Locate every Plasmodium ovale-infected red blood cell.
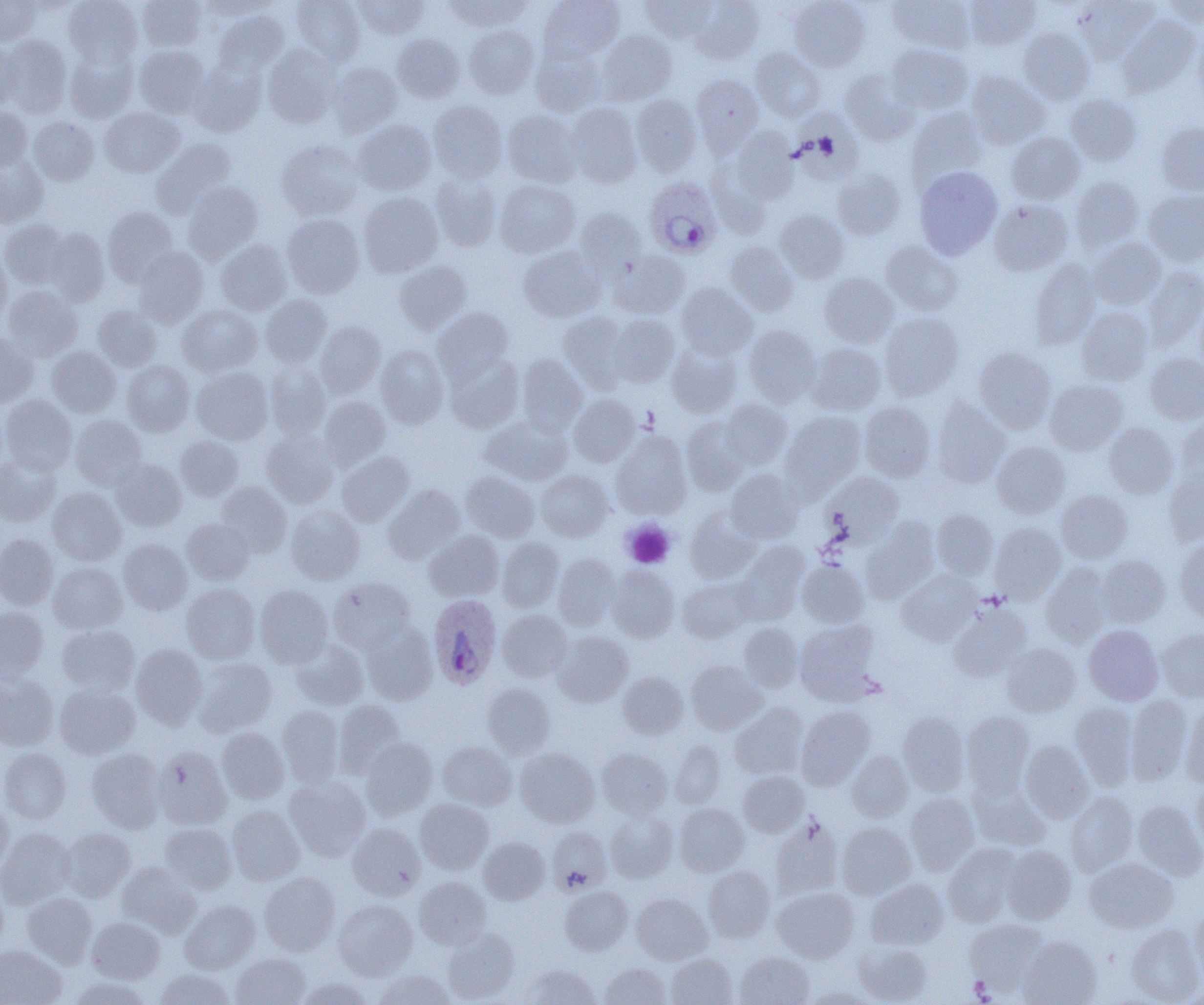
Approximate bounding boxes as named x1/y1/x2/y2 corners in pixels.
Plasmodium ovale-infected red blood cells: (x1=644, y1=177, x2=723, y2=259), (x1=428, y1=594, x2=502, y2=690).

Summary:
  - Platelet locations: (x1=622, y1=520, x2=675, y2=568), (x1=969, y1=976, x2=994, y2=1001)
  - Uninfected red blood cell locations: (x1=0, y1=0, x2=41, y2=44), (x1=64, y1=0, x2=142, y2=67), (x1=201, y1=0, x2=279, y2=20), (x1=292, y1=0, x2=365, y2=65), (x1=353, y1=0, x2=429, y2=39), (x1=446, y1=0, x2=531, y2=31), (x1=539, y1=0, x2=625, y2=61), (x1=641, y1=0, x2=716, y2=42), (x1=690, y1=0, x2=765, y2=63), (x1=888, y1=0, x2=976, y2=54), (x1=964, y1=0, x2=1040, y2=50), (x1=1074, y1=0, x2=1158, y2=63), (x1=1162, y1=0, x2=1204, y2=27), (x1=137, y1=1, x2=207, y2=51), (x1=789, y1=1, x2=870, y2=71), (x1=213, y1=10, x2=289, y2=76), (x1=1118, y1=16, x2=1200, y2=97), (x1=464, y1=25, x2=538, y2=99), (x1=1193, y1=27, x2=1204, y2=104), (x1=1018, y1=28, x2=1094, y2=104), (x1=596, y1=30, x2=677, y2=105), (x1=392, y1=34, x2=464, y2=103), (x1=2, y1=36, x2=72, y2=118), (x1=0, y1=43, x2=22, y2=109), (x1=887, y1=43, x2=973, y2=114), (x1=263, y1=44, x2=343, y2=126), (x1=135, y1=45, x2=210, y2=118), (x1=530, y1=45, x2=605, y2=116), (x1=751, y1=47, x2=826, y2=121), (x1=64, y1=48, x2=138, y2=122), (x1=190, y1=61, x2=266, y2=136), (x1=329, y1=62, x2=403, y2=136), (x1=839, y1=67, x2=919, y2=144), (x1=967, y1=72, x2=1050, y2=149), (x1=691, y1=74, x2=763, y2=153), (x1=631, y1=93, x2=702, y2=176), (x1=1066, y1=93, x2=1141, y2=166), (x1=428, y1=101, x2=507, y2=182), (x1=565, y1=102, x2=643, y2=188), (x1=100, y1=106, x2=185, y2=177), (x1=0, y1=107, x2=32, y2=172), (x1=907, y1=108, x2=988, y2=186), (x1=790, y1=109, x2=865, y2=183), (x1=502, y1=110, x2=581, y2=186), (x1=29, y1=117, x2=99, y2=185), (x1=354, y1=119, x2=437, y2=194), (x1=1157, y1=122, x2=1204, y2=195), (x1=730, y1=127, x2=799, y2=202), (x1=1007, y1=131, x2=1085, y2=204), (x1=151, y1=138, x2=236, y2=217), (x1=277, y1=139, x2=364, y2=219), (x1=0, y1=158, x2=48, y2=227), (x1=707, y1=160, x2=776, y2=238), (x1=914, y1=166, x2=1002, y2=258), (x1=832, y1=169, x2=906, y2=239), (x1=430, y1=173, x2=501, y2=251), (x1=1071, y1=177, x2=1143, y2=252), (x1=494, y1=179, x2=580, y2=258), (x1=183, y1=182, x2=263, y2=262), (x1=1144, y1=188, x2=1204, y2=266), (x1=358, y1=192, x2=443, y2=277), (x1=990, y1=199, x2=1072, y2=275), (x1=102, y1=207, x2=179, y2=284), (x1=574, y1=208, x2=647, y2=280), (x1=774, y1=209, x2=849, y2=281), (x1=282, y1=214, x2=364, y2=298), (x1=0, y1=219, x2=69, y2=288), (x1=44, y1=228, x2=110, y2=305), (x1=1087, y1=237, x2=1166, y2=309), (x1=215, y1=240, x2=292, y2=315), (x1=881, y1=241, x2=964, y2=316), (x1=725, y1=242, x2=798, y2=316), (x1=134, y1=246, x2=208, y2=326), (x1=518, y1=246, x2=604, y2=322), (x1=0, y1=249, x2=11, y2=325), (x1=609, y1=251, x2=690, y2=319), (x1=1029, y1=259, x2=1100, y2=348), (x1=394, y1=260, x2=471, y2=333), (x1=1143, y1=266, x2=1204, y2=349), (x1=819, y1=273, x2=898, y2=347), (x1=676, y1=283, x2=758, y2=359), (x1=3, y1=286, x2=83, y2=360), (x1=261, y1=294, x2=332, y2=367), (x1=1195, y1=300, x2=1204, y2=374), (x1=93, y1=304, x2=162, y2=371), (x1=177, y1=304, x2=261, y2=376), (x1=1077, y1=307, x2=1153, y2=384), (x1=432, y1=308, x2=513, y2=381), (x1=558, y1=311, x2=629, y2=390), (x1=879, y1=312, x2=964, y2=400), (x1=609, y1=315, x2=681, y2=387), (x1=315, y1=321, x2=385, y2=397), (x1=744, y1=325, x2=821, y2=406), (x1=0, y1=333, x2=38, y2=407), (x1=666, y1=342, x2=741, y2=417), (x1=808, y1=343, x2=886, y2=415), (x1=376, y1=344, x2=449, y2=428), (x1=47, y1=346, x2=121, y2=417), (x1=974, y1=347, x2=1056, y2=433), (x1=445, y1=353, x2=524, y2=434), (x1=1145, y1=354, x2=1204, y2=424), (x1=517, y1=355, x2=588, y2=433), (x1=122, y1=360, x2=195, y2=436), (x1=265, y1=361, x2=330, y2=440), (x1=192, y1=367, x2=273, y2=445), (x1=1044, y1=379, x2=1127, y2=455), (x1=569, y1=394, x2=640, y2=466), (x1=1, y1=395, x2=77, y2=474), (x1=318, y1=396, x2=390, y2=470), (x1=932, y1=398, x2=1009, y2=487), (x1=720, y1=399, x2=793, y2=468), (x1=859, y1=401, x2=935, y2=481), (x1=782, y1=411, x2=866, y2=492), (x1=482, y1=415, x2=573, y2=485), (x1=70, y1=416, x2=147, y2=490), (x1=681, y1=416, x2=752, y2=494), (x1=1175, y1=417, x2=1204, y2=489), (x1=1104, y1=422, x2=1178, y2=499), (x1=261, y1=430, x2=340, y2=508), (x1=612, y1=431, x2=691, y2=518), (x1=175, y1=435, x2=243, y2=501), (x1=992, y1=441, x2=1070, y2=518), (x1=337, y1=451, x2=415, y2=526), (x1=0, y1=454, x2=61, y2=526), (x1=111, y1=460, x2=187, y2=531), (x1=726, y1=469, x2=804, y2=543), (x1=1163, y1=469, x2=1204, y2=546), (x1=536, y1=470, x2=613, y2=542), (x1=461, y1=471, x2=540, y2=542), (x1=822, y1=472, x2=903, y2=544), (x1=216, y1=482, x2=292, y2=557), (x1=383, y1=485, x2=465, y2=564), (x1=47, y1=487, x2=127, y2=565), (x1=1057, y1=491, x2=1132, y2=562), (x1=286, y1=505, x2=364, y2=584), (x1=685, y1=509, x2=760, y2=583), (x1=931, y1=509, x2=998, y2=579), (x1=182, y1=518, x2=254, y2=584), (x1=861, y1=520, x2=938, y2=603), (x1=990, y1=522, x2=1066, y2=603), (x1=424, y1=530, x2=504, y2=601), (x1=0, y1=534, x2=58, y2=610), (x1=497, y1=537, x2=563, y2=612), (x1=1175, y1=538, x2=1204, y2=622), (x1=118, y1=539, x2=192, y2=614), (x1=734, y1=542, x2=809, y2=623), (x1=552, y1=552, x2=620, y2=630), (x1=1096, y1=555, x2=1170, y2=626), (x1=797, y1=560, x2=868, y2=627), (x1=48, y1=562, x2=127, y2=634), (x1=1041, y1=564, x2=1110, y2=647), (x1=606, y1=565, x2=680, y2=643), (x1=898, y1=571, x2=980, y2=646), (x1=677, y1=577, x2=755, y2=642), (x1=329, y1=578, x2=416, y2=652), (x1=181, y1=584, x2=260, y2=663), (x1=255, y1=585, x2=333, y2=667), (x1=949, y1=603, x2=1032, y2=680), (x1=0, y1=607, x2=49, y2=683), (x1=498, y1=610, x2=572, y2=681), (x1=795, y1=620, x2=880, y2=705), (x1=362, y1=623, x2=438, y2=704), (x1=739, y1=623, x2=803, y2=692), (x1=1084, y1=624, x2=1163, y2=705), (x1=57, y1=625, x2=139, y2=696), (x1=1157, y1=627, x2=1204, y2=701), (x1=553, y1=632, x2=633, y2=706), (x1=289, y1=639, x2=369, y2=710), (x1=1001, y1=643, x2=1080, y2=718), (x1=130, y1=644, x2=208, y2=729), (x1=194, y1=658, x2=278, y2=737), (x1=686, y1=660, x2=766, y2=734), (x1=618, y1=672, x2=688, y2=739), (x1=0, y1=675, x2=58, y2=750), (x1=482, y1=683, x2=556, y2=757), (x1=55, y1=684, x2=139, y2=758), (x1=1126, y1=694, x2=1192, y2=783), (x1=333, y1=700, x2=407, y2=777), (x1=1071, y1=702, x2=1139, y2=788), (x1=730, y1=703, x2=808, y2=778), (x1=1181, y1=703, x2=1204, y2=788), (x1=277, y1=705, x2=345, y2=787), (x1=796, y1=706, x2=875, y2=789), (x1=898, y1=711, x2=969, y2=795), (x1=960, y1=711, x2=1035, y2=794), (x1=216, y1=727, x2=290, y2=803), (x1=361, y1=738, x2=438, y2=819), (x1=670, y1=739, x2=726, y2=808), (x1=1021, y1=740, x2=1093, y2=822), (x1=437, y1=741, x2=517, y2=811), (x1=153, y1=746, x2=232, y2=830), (x1=0, y1=748, x2=71, y2=823), (x1=85, y1=748, x2=165, y2=832), (x1=515, y1=748, x2=599, y2=827), (x1=596, y1=748, x2=672, y2=819), (x1=847, y1=751, x2=914, y2=821), (x1=738, y1=771, x2=809, y2=837), (x1=284, y1=776, x2=371, y2=860), (x1=970, y1=781, x2=1049, y2=851), (x1=1192, y1=781, x2=1204, y2=854), (x1=905, y1=792, x2=980, y2=874), (x1=1065, y1=792, x2=1138, y2=875), (x1=0, y1=799, x2=12, y2=874), (x1=415, y1=799, x2=494, y2=874), (x1=1133, y1=800, x2=1204, y2=880), (x1=674, y1=803, x2=749, y2=876), (x1=227, y1=805, x2=304, y2=885), (x1=605, y1=809, x2=678, y2=882), (x1=771, y1=817, x2=845, y2=900), (x1=836, y1=822, x2=916, y2=899), (x1=159, y1=823, x2=237, y2=893), (x1=347, y1=823, x2=425, y2=899), (x1=61, y1=827, x2=136, y2=901), (x1=546, y1=827, x2=611, y2=894), (x1=0, y1=828, x2=75, y2=909), (x1=478, y1=837, x2=549, y2=904), (x1=943, y1=843, x2=1022, y2=927), (x1=1001, y1=845, x2=1076, y2=924), (x1=1085, y1=857, x2=1177, y2=932), (x1=116, y1=862, x2=200, y2=937), (x1=704, y1=866, x2=775, y2=943), (x1=259, y1=872, x2=340, y2=955), (x1=414, y1=876, x2=492, y2=949), (x1=866, y1=879, x2=948, y2=949), (x1=0, y1=880, x2=9, y2=957), (x1=560, y1=886, x2=633, y2=955), (x1=772, y1=886, x2=859, y2=962), (x1=22, y1=892, x2=97, y2=967), (x1=631, y1=892, x2=712, y2=964), (x1=180, y1=900, x2=259, y2=973), (x1=333, y1=900, x2=417, y2=980), (x1=1191, y1=906, x2=1204, y2=981), (x1=87, y1=916, x2=165, y2=983), (x1=965, y1=918, x2=1049, y2=995), (x1=1127, y1=923, x2=1203, y2=1004), (x1=443, y1=928, x2=519, y2=1003), (x1=1018, y1=936, x2=1102, y2=1005), (x1=854, y1=941, x2=933, y2=1004), (x1=0, y1=945, x2=66, y2=1005), (x1=734, y1=951, x2=815, y2=1005), (x1=231, y1=953, x2=311, y2=1005), (x1=665, y1=953, x2=738, y2=1004), (x1=599, y1=962, x2=670, y2=1005), (x1=520, y1=963, x2=600, y2=1005), (x1=155, y1=968, x2=236, y2=1005), (x1=374, y1=969, x2=456, y2=1005), (x1=69, y1=975, x2=152, y2=1005), (x1=296, y1=977, x2=374, y2=1005), (x1=802, y1=986, x2=877, y2=1005)
  - Slide-level diagnosis: Plasmodium ovale
  - Magnification: 1000x
  - Field of view: one of a larger specimen
  - Modality: optical microscopy
  - Preparation: thin blood smear
  - Image size: 1204×1005 pixels